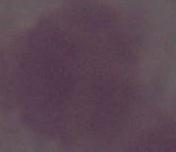
An erythrocyte is shown. Micrograph. 1000x magnification.